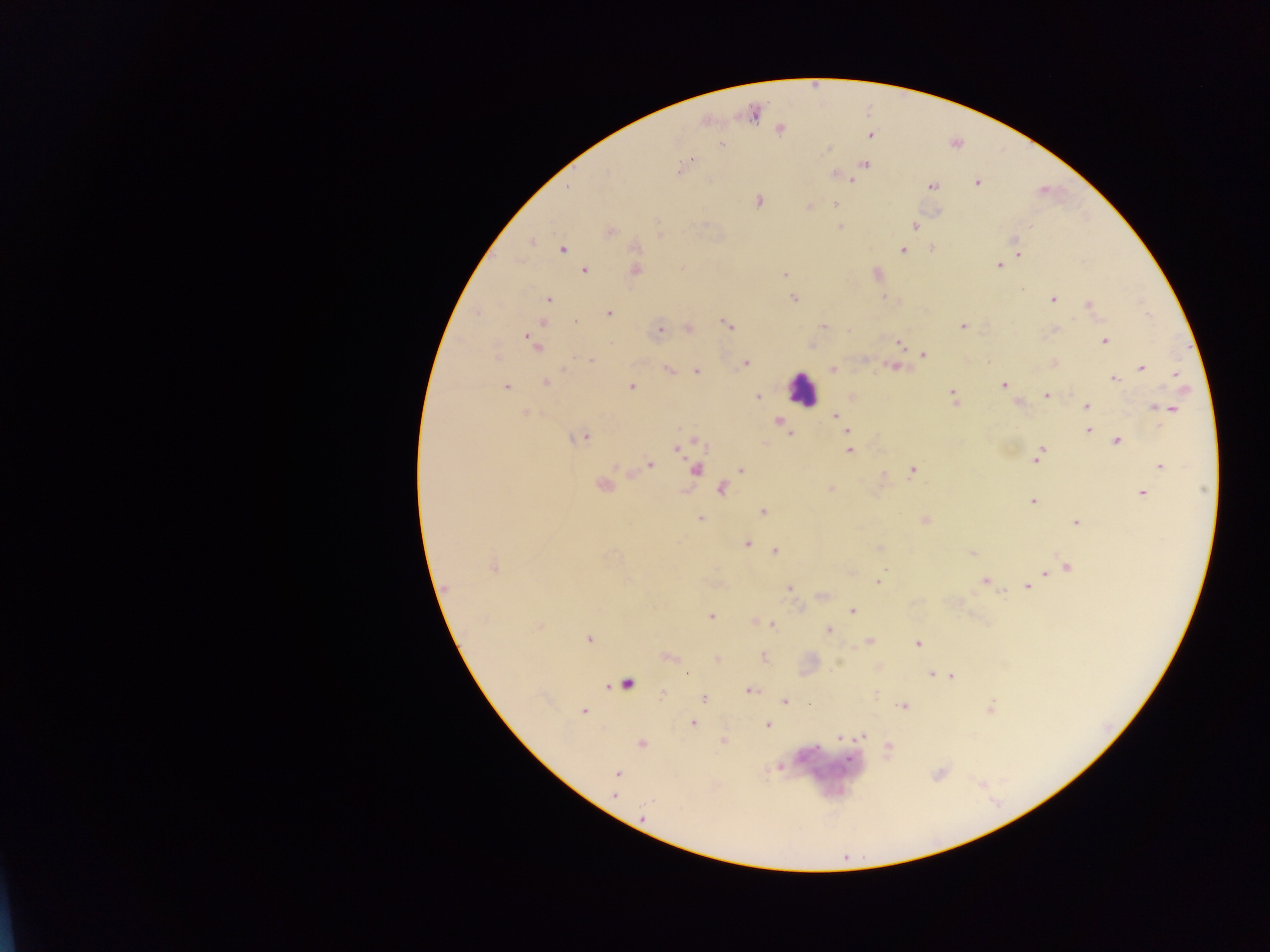
leukocyte locations = approximate centers as x y in pixels: 802 388
preparation = thick blood smear
image size = 1270×952 pixels
Plasmodium parasite locations = approximate centers as x y in pixels: 780 129; 870 135; 722 144; 828 150; 690 162; 864 165; 682 168; 608 173; 835 175; 853 180; 977 183; 933 185; 758 201; 836 204; 809 207; 840 226; 915 226; 1030 227; 609 231; 532 241; 635 247; 562 248; 931 249; 902 250; 1018 255; 999 265; 585 271; 635 271; 785 275; 876 275; 1021 289; 794 298; 883 298; 548 299; 1053 299; 1088 305; 608 313; 543 322; 576 322; 728 325; 962 326; 823 327; 688 328; 659 332; 529 337; 1105 341; 899 344; 536 345; 923 355; 590 360; 746 363; 1054 363; 893 366; 1142 367; 668 369; 833 369; 696 371; 1176 374; 1113 379; 545 382; 1003 385; 506 387; 631 387; 757 396; 953 396; 1047 396; 1087 406; 1170 409; 524 414; 835 415; 779 422; 1088 431; 789 435; 584 438; 1117 441; 696 442; 678 448; 848 450; 1041 450; 1037 458; 650 465; 1160 466; 696 469; 741 469; 913 471; 602 485; 722 489; 830 490; 1142 493; 1033 501; 763 512; 700 517; 924 521; 1076 522; 747 543; 879 547; 775 551; 972 554; 1068 566; 494 568; 1045 574; 1038 577; 985 581; 878 582; 1028 586; 789 588; 447 589; 822 596; 852 611; 711 617; 754 622; 772 626; 541 627; 828 631; 589 639; 869 641; 918 643; 763 657; 717 658; 686 673; 930 674; 951 676; 626 684; 749 691; 662 693; 704 699; 784 701; 902 707; 584 712; 692 724; 767 725; 841 737; 862 737; 723 740; 641 744; 888 748; 617 774; 614 795
country = Ghana
field of view = single
capture = mobile-phone photograph through a microscope